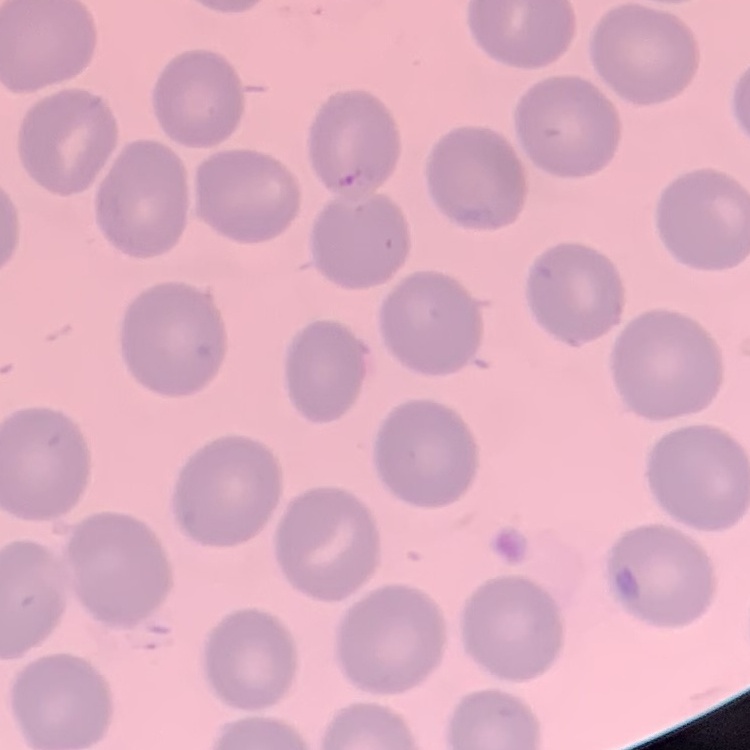
The erythrocytes show no rouleaux formation. Thin peripheral smear. Stained with either Field's or Giemsa. One tile cut from a larger photomicrograph.